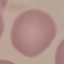 Malaria status: uninfected. Giemsa stain. Thin blood film. Acquired by smartphone through the microscope eyepiece. Automatically extracted cell patch, resized to 64 × 64 pixels.